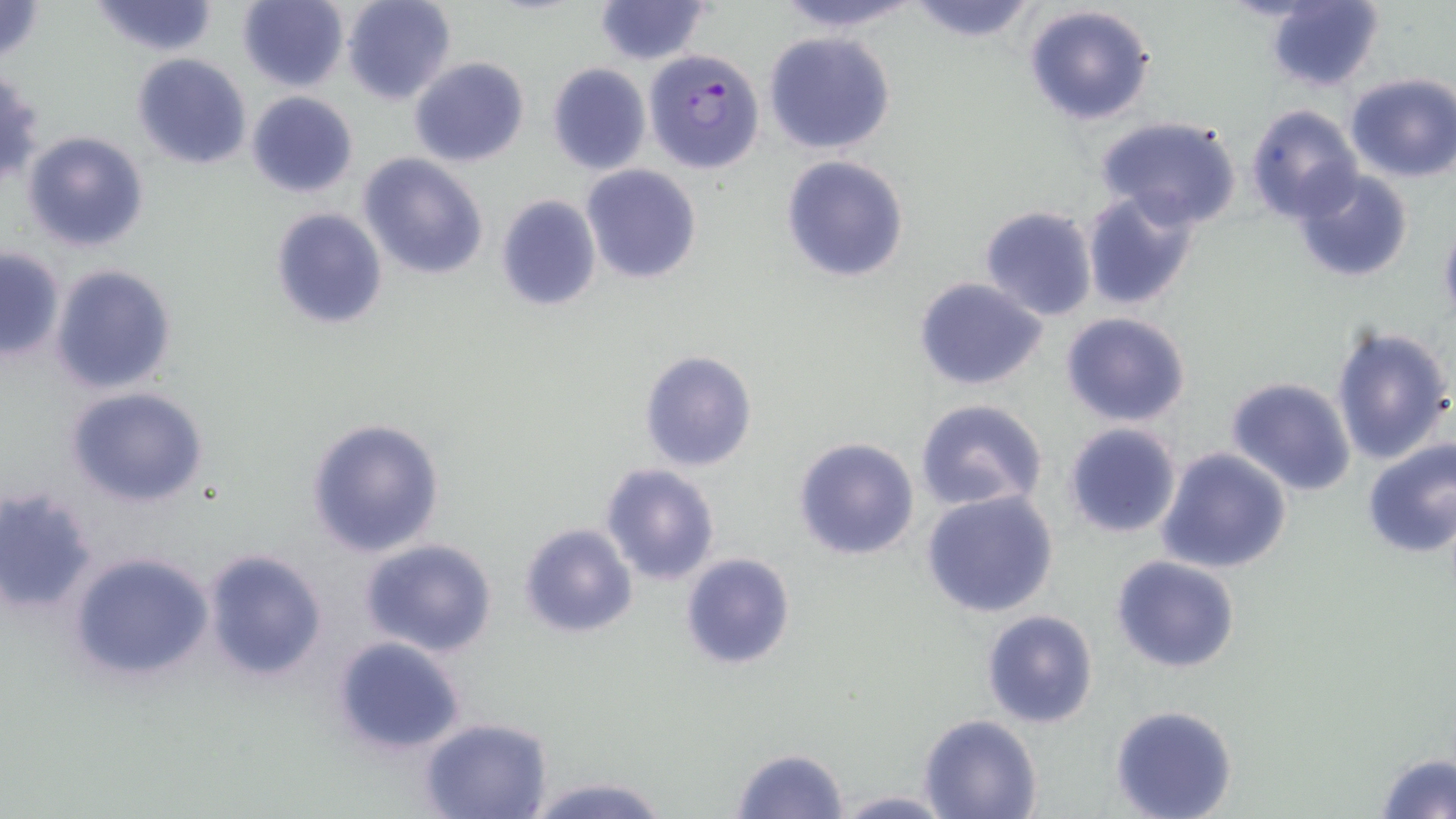

slide-level diagnosis = Plasmodium falciparum
magnification = 1000x
image size = 1456×819 pixels
stain = May-Grünwald-Giemsa
modality = optical microscopy
uninfected red blood cell locations = approximate bounding boxes as [x1, y1, x2, y2] in pixels: [0, 0, 47, 63], [91, 0, 219, 57], [238, 0, 349, 90], [341, 0, 455, 105], [767, 0, 921, 34], [904, 0, 1039, 43], [594, 1, 712, 66], [1264, 1, 1385, 90], [1022, 4, 1156, 126], [763, 32, 896, 156], [132, 53, 251, 169], [408, 56, 530, 168], [546, 62, 651, 174], [0, 71, 45, 188], [1343, 72, 1455, 182], [246, 90, 358, 198], [1244, 104, 1363, 223], [1095, 115, 1243, 229], [21, 130, 149, 252], [359, 153, 489, 280], [780, 155, 909, 282], [580, 166, 702, 284], [1289, 167, 1416, 284], [1080, 188, 1201, 311], [496, 195, 602, 311], [978, 206, 1098, 321], [268, 207, 388, 330], [1437, 217, 1456, 331], [0, 249, 65, 360], [50, 263, 178, 395], [913, 275, 1049, 392], [1059, 311, 1192, 428], [1330, 324, 1454, 465], [639, 349, 758, 472], [1226, 377, 1358, 496], [65, 387, 210, 508], [914, 399, 1050, 515], [304, 417, 445, 558], [1063, 423, 1181, 538], [793, 435, 920, 562], [1359, 437, 1456, 557], [1155, 447, 1294, 573], [600, 463, 721, 586], [1, 487, 100, 615], [920, 489, 1062, 617], [517, 522, 638, 639], [357, 538, 499, 658], [203, 549, 327, 683], [67, 551, 217, 683], [679, 553, 796, 672], [1111, 555, 1242, 675], [980, 609, 1099, 728], [330, 635, 471, 756], [1109, 704, 1238, 819], [918, 714, 1043, 819], [420, 717, 552, 819], [731, 747, 849, 818], [1375, 752, 1455, 819], [526, 774, 670, 819], [831, 791, 955, 818]
preparation = thin blood film
Plasmodium falciparum-infected red blood cell locations = approximate bounding boxes as [x1, y1, x2, y2] in pixels: [645, 48, 764, 174]
field of view = one of a larger specimen